Name the blood parasite species.
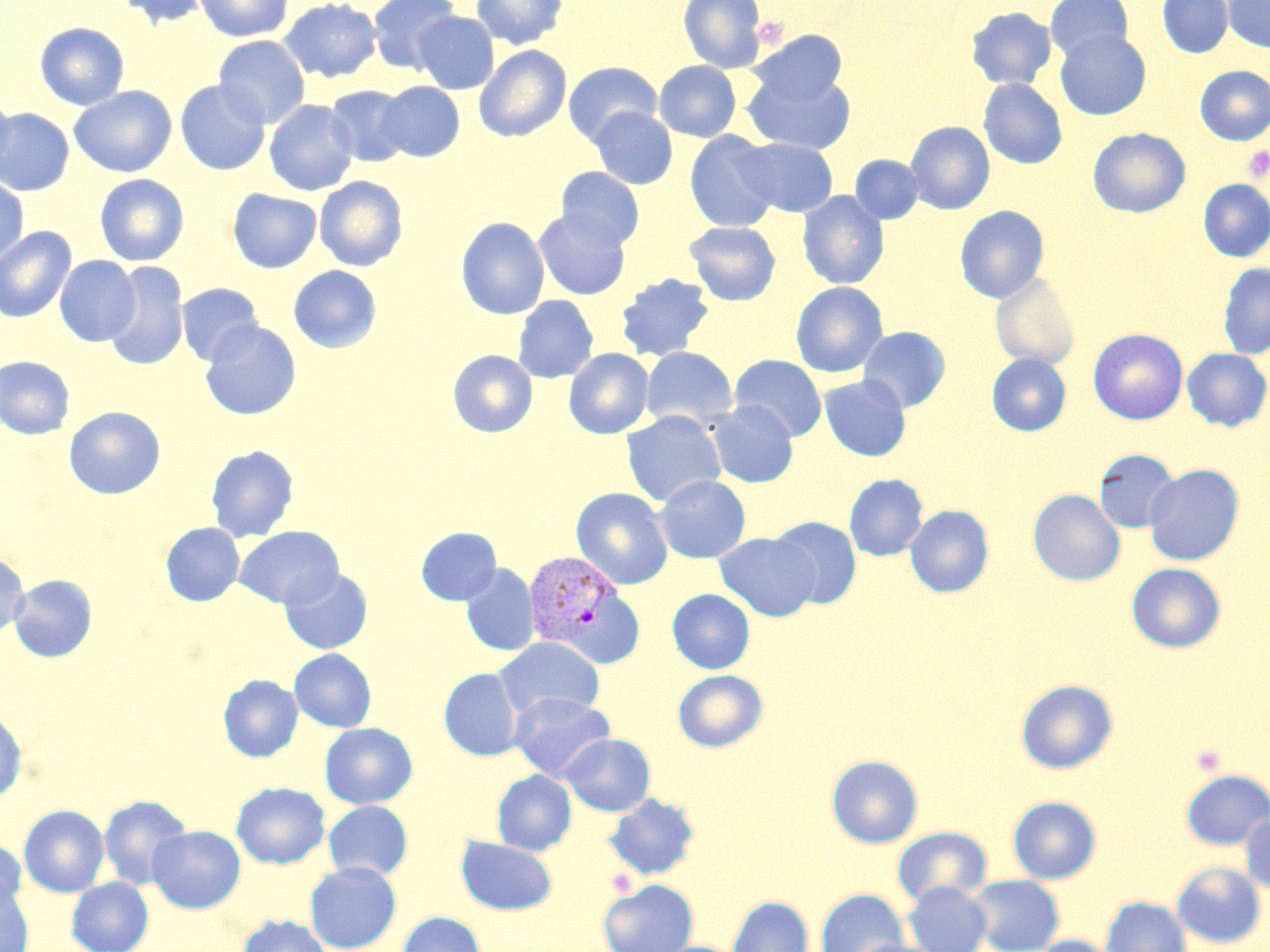

Plasmodium vivax.

stain = May-Grünwald-Giemsa
field of view = single
Plasmodium vivax-infected red blood cell locations = approximate bounding boxes as [x1, y1, x2, y2] in pixels: [523, 550, 632, 661]
uninfected red blood cell locations = approximate bounding boxes as [x1, y1, x2, y2] in pixels: [112, 0, 211, 29], [279, 0, 382, 83], [367, 0, 461, 75], [470, 0, 569, 50], [678, 0, 766, 72], [1044, 0, 1133, 63], [1157, 0, 1233, 58], [1223, 0, 1270, 53], [195, 1, 293, 42], [965, 7, 1057, 91], [414, 11, 499, 94], [34, 22, 130, 110], [747, 31, 848, 107], [1055, 31, 1151, 121], [213, 35, 310, 128], [473, 45, 572, 143], [563, 61, 662, 146], [654, 61, 741, 142], [1195, 66, 1270, 145], [743, 67, 856, 155], [978, 79, 1067, 169], [175, 80, 271, 176], [376, 82, 464, 162], [69, 85, 177, 178], [325, 85, 413, 167], [0, 92, 16, 181], [264, 100, 358, 196], [589, 107, 678, 190], [0, 108, 75, 197], [906, 122, 995, 215], [1088, 128, 1190, 218], [684, 131, 781, 232], [739, 139, 838, 217], [850, 155, 923, 224], [556, 167, 645, 250], [94, 174, 189, 266], [0, 176, 28, 265], [315, 176, 408, 272], [1198, 180, 1270, 261], [227, 188, 322, 273], [798, 191, 889, 289], [955, 205, 1049, 304], [533, 210, 631, 300], [456, 217, 549, 319], [684, 221, 781, 306], [0, 227, 76, 323], [54, 255, 140, 347], [102, 262, 189, 371], [1217, 262, 1270, 359], [288, 265, 382, 353], [990, 273, 1080, 370], [615, 274, 715, 361], [790, 281, 888, 377], [176, 283, 264, 367], [512, 295, 599, 383], [199, 321, 302, 420], [858, 326, 950, 413], [1088, 329, 1188, 424], [641, 347, 738, 431], [563, 348, 654, 439], [1182, 348, 1270, 431], [448, 350, 537, 438], [986, 354, 1071, 436], [729, 355, 828, 442], [0, 356, 75, 439], [819, 375, 911, 461], [706, 402, 798, 488], [64, 406, 166, 500], [621, 410, 726, 507], [205, 444, 299, 543], [1094, 449, 1181, 533], [1144, 463, 1244, 566], [844, 474, 928, 562], [655, 475, 751, 564], [570, 487, 673, 590], [1028, 489, 1125, 586], [905, 505, 994, 597], [767, 515, 861, 609], [160, 523, 244, 606], [233, 526, 344, 608], [415, 527, 502, 605], [714, 532, 819, 621], [0, 552, 30, 637], [1126, 562, 1227, 653], [460, 564, 540, 656], [279, 567, 373, 655], [9, 575, 97, 662], [667, 588, 755, 674], [494, 637, 605, 722], [289, 649, 377, 732], [440, 668, 524, 761], [673, 670, 768, 752], [218, 674, 303, 762], [1016, 679, 1118, 774], [509, 692, 614, 781], [0, 711, 27, 801], [319, 723, 418, 809], [561, 734, 655, 816], [826, 755, 923, 848], [1181, 769, 1270, 850], [492, 770, 576, 856], [232, 782, 330, 869], [604, 793, 700, 880], [98, 795, 193, 891], [1008, 796, 1101, 884], [323, 801, 413, 880], [19, 805, 110, 897], [1239, 812, 1270, 895], [147, 825, 245, 913], [892, 826, 992, 906], [456, 836, 557, 915], [0, 839, 27, 915], [305, 861, 402, 952], [1170, 861, 1267, 949], [967, 874, 1064, 952], [67, 876, 153, 952], [598, 879, 698, 952], [0, 881, 33, 952], [903, 881, 991, 952], [816, 888, 910, 952], [727, 895, 814, 952], [1100, 896, 1191, 952], [396, 912, 486, 952], [236, 914, 333, 952], [1031, 935, 1117, 952], [844, 938, 948, 952]
platelet locations = approximate bounding boxes as [x1, y1, x2, y2] in pixels: [753, 17, 787, 48], [1242, 145, 1270, 183], [1190, 745, 1226, 776], [604, 869, 640, 898]
preparation = thin blood film
image size = 1270×952 pixels
modality = light microscopy
magnification = 1000x